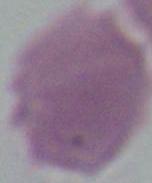
Summary:
  - Magnification: 1000x
  - Modality: photomicrograph
  - Identification: erythrocyte